Give the extent of all uninfected red blood cells.
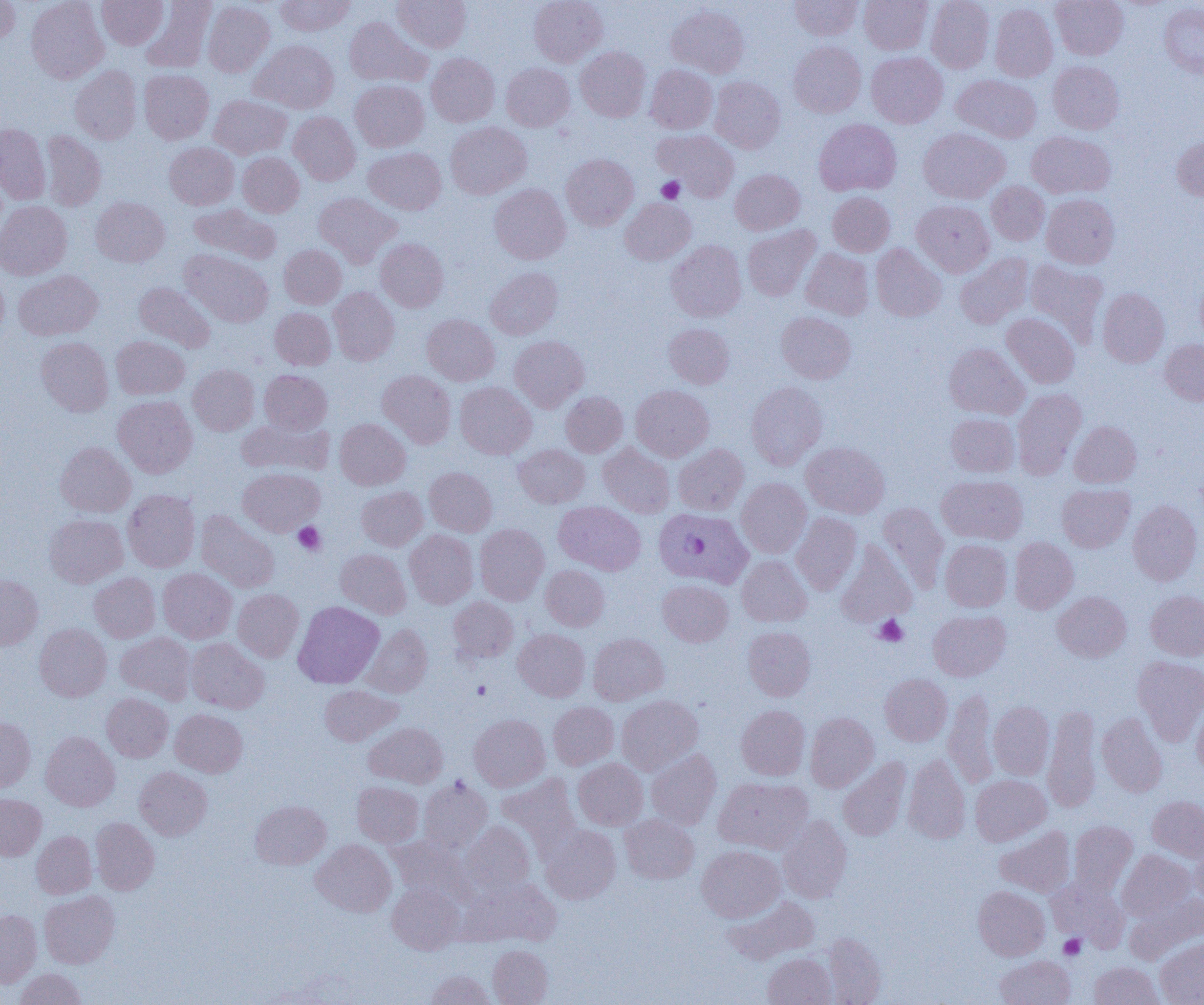
Approximate bounding boxes as [x1, y1, x2, y2] in pixels.
Uninfected red blood cells: [26, 0, 108, 83], [97, 0, 168, 49], [275, 0, 356, 36], [392, 0, 471, 52], [529, 0, 608, 67], [789, 0, 863, 40], [859, 0, 932, 54], [926, 0, 994, 73], [1051, 0, 1128, 60], [0, 1, 21, 46], [141, 1, 216, 73], [203, 1, 275, 77], [1159, 2, 1204, 79], [990, 3, 1058, 82], [666, 5, 749, 78], [345, 16, 431, 88], [250, 40, 338, 113], [788, 41, 866, 117], [576, 46, 650, 122], [866, 51, 947, 128], [427, 53, 499, 127], [1048, 60, 1124, 134], [501, 63, 575, 131], [645, 65, 717, 134], [70, 66, 141, 144], [139, 69, 214, 144], [952, 75, 1041, 143], [709, 76, 785, 153], [350, 80, 428, 151], [209, 95, 292, 159], [289, 112, 360, 185], [814, 118, 901, 196], [446, 121, 532, 199], [0, 124, 50, 204], [918, 128, 1009, 203], [653, 129, 739, 201], [40, 131, 107, 211], [1027, 131, 1115, 198], [1171, 135, 1204, 200], [164, 142, 239, 209], [363, 147, 446, 214], [238, 152, 305, 217], [561, 154, 638, 230], [730, 169, 805, 234], [987, 181, 1049, 245], [489, 184, 570, 264], [313, 192, 402, 267], [828, 192, 894, 256], [1041, 194, 1119, 269], [91, 197, 170, 267], [620, 198, 696, 265], [912, 200, 994, 277], [0, 201, 72, 279], [189, 203, 281, 264], [742, 226, 820, 301], [375, 238, 448, 312], [666, 240, 746, 322], [870, 244, 946, 321], [279, 245, 346, 308], [801, 248, 874, 320], [180, 249, 273, 327], [955, 253, 1033, 329], [1026, 259, 1108, 345], [0, 267, 9, 345], [485, 267, 563, 339], [13, 269, 103, 340], [134, 281, 216, 352], [328, 287, 399, 365], [1098, 288, 1169, 367], [270, 307, 336, 369], [777, 311, 856, 384], [1002, 313, 1079, 388], [422, 314, 500, 385], [664, 323, 734, 388], [111, 336, 189, 399], [510, 336, 589, 412], [36, 337, 113, 416], [1160, 339, 1204, 406], [944, 343, 1029, 420], [188, 365, 259, 435], [377, 369, 456, 448], [260, 370, 332, 433], [455, 381, 536, 458], [746, 381, 827, 469], [631, 385, 714, 461], [1012, 389, 1086, 478], [561, 391, 627, 457], [113, 395, 198, 477], [945, 413, 1019, 477], [237, 417, 333, 477], [335, 419, 411, 490], [1069, 421, 1142, 488], [56, 442, 135, 517], [801, 442, 889, 518], [599, 443, 675, 517], [514, 444, 590, 507], [673, 444, 749, 515], [238, 467, 325, 536], [424, 467, 497, 536], [936, 475, 1028, 545], [737, 478, 811, 557], [1057, 484, 1135, 552], [356, 486, 428, 551], [122, 489, 200, 572], [1128, 499, 1203, 585], [554, 501, 646, 575], [878, 502, 949, 592], [196, 511, 280, 592], [791, 512, 862, 594], [44, 514, 128, 587], [475, 524, 549, 605], [405, 530, 478, 608], [1009, 537, 1078, 614], [940, 540, 1012, 611], [836, 541, 916, 626], [335, 549, 411, 618], [737, 555, 812, 626], [540, 565, 610, 631], [158, 568, 237, 643], [89, 573, 160, 642], [0, 575, 43, 649], [657, 580, 733, 646], [233, 589, 304, 662], [1053, 591, 1131, 662], [1146, 591, 1204, 660], [449, 597, 518, 662], [294, 601, 384, 688], [929, 609, 1011, 681], [34, 623, 112, 701], [361, 624, 433, 697], [743, 626, 815, 700], [513, 629, 589, 701], [116, 632, 196, 704], [588, 633, 669, 705], [186, 638, 269, 713], [1132, 655, 1204, 745], [880, 673, 952, 746], [319, 685, 402, 746], [943, 689, 999, 787], [102, 693, 173, 762], [617, 695, 703, 775], [988, 701, 1054, 780], [1192, 701, 1204, 776], [549, 702, 619, 769], [736, 705, 810, 780], [1043, 705, 1102, 813], [170, 708, 247, 777], [806, 712, 878, 791], [1097, 712, 1167, 797], [469, 714, 550, 791], [0, 716, 35, 791], [364, 722, 447, 788], [40, 731, 120, 811], [646, 749, 721, 829], [903, 755, 971, 844], [838, 757, 911, 841], [573, 758, 647, 830], [134, 767, 212, 840], [497, 773, 581, 854], [970, 774, 1050, 846], [418, 777, 492, 853], [714, 777, 813, 854], [352, 781, 424, 847], [0, 794, 46, 860], [1147, 796, 1204, 862], [250, 800, 331, 869], [620, 814, 699, 883], [777, 816, 852, 903], [90, 817, 160, 895], [1069, 820, 1137, 895], [460, 821, 535, 897], [541, 825, 620, 904], [995, 826, 1076, 897], [32, 831, 96, 898], [389, 836, 469, 902], [311, 839, 396, 917], [1190, 840, 1204, 907], [697, 845, 785, 922], [1117, 850, 1195, 921], [1048, 878, 1128, 951], [461, 879, 560, 947], [387, 883, 464, 953], [973, 886, 1050, 960], [39, 890, 120, 968], [1129, 893, 1204, 962], [723, 896, 818, 964], [0, 909, 42, 987], [821, 932, 887, 1004], [1155, 937, 1204, 1005], [488, 945, 553, 1005], [763, 953, 836, 1005], [995, 955, 1075, 1005], [1089, 961, 1163, 1005], [15, 968, 86, 1005], [424, 970, 496, 1004].

Platelet locations: [657, 176, 685, 203], [293, 522, 325, 555], [874, 615, 908, 647], [472, 680, 491, 700], [1059, 934, 1086, 960]. Plasmodium falciparum-infected red blood cell locations: [653, 507, 753, 587]. Slide-level diagnosis: Plasmodium falciparum. 1000x magnification. Single field of view. Image is 1204×1005 pixels. Thin blood film. Optical microscopy.